Name the parasite shown.
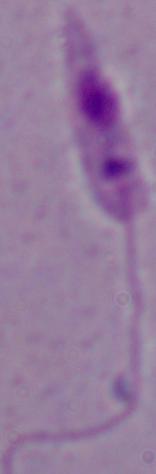
Leishmania.

Captured at 1000x magnification. Micrograph.